Identify the parasite.
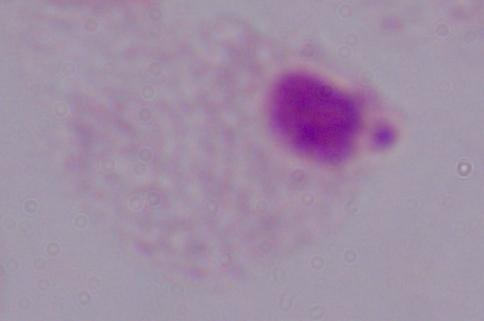

A trichomonad.

1000x magnification. Photomicrograph.